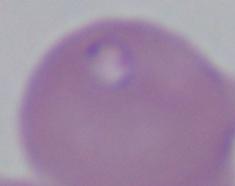
magnification: 1000x
identification: Babesia
modality: photomicrograph